Identify the parasite.
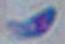
This is Toxoplasma gondii.

modality = micrograph
magnification = 1000x